Locate the cells, classifying each as a parasitized RBC, an uninfected RBC, or a WBC.
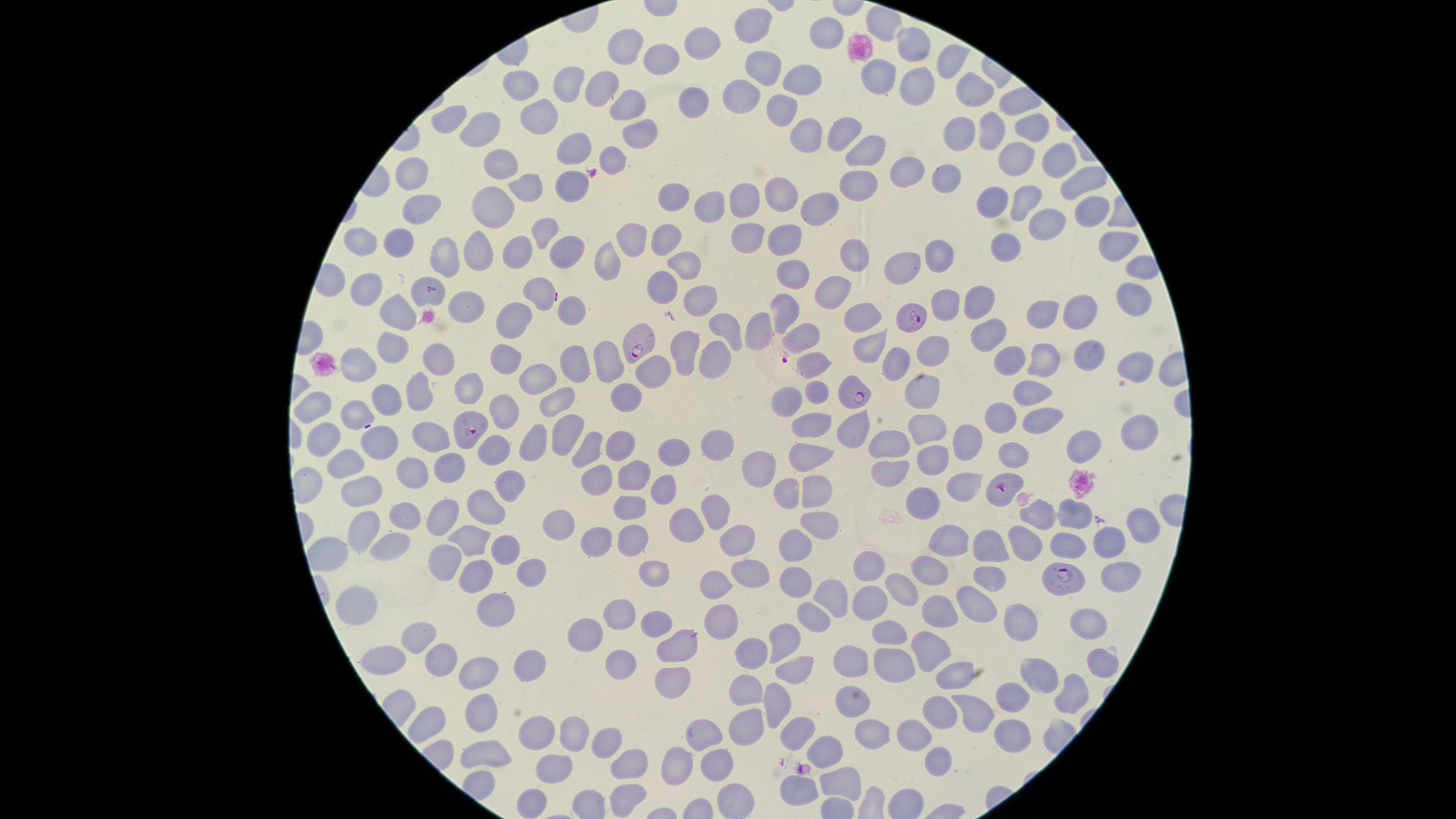

Approximate marker points, in pixels from the top-left corner.
Parasitized RBCs: (x=912, y=319), (x=646, y=343), (x=852, y=388), (x=468, y=427), (x=997, y=487), (x=1062, y=578).
Uninfected RBCs: (x=883, y=24), (x=753, y=29), (x=823, y=31), (x=696, y=45), (x=920, y=45), (x=627, y=50), (x=666, y=59), (x=948, y=60), (x=762, y=63), (x=882, y=74), (x=791, y=78), (x=916, y=81), (x=970, y=84), (x=605, y=86), (x=518, y=89), (x=562, y=91), (x=742, y=91), (x=693, y=99), (x=628, y=106), (x=781, y=111), (x=542, y=120), (x=451, y=125), (x=1030, y=125), (x=486, y=128), (x=811, y=128), (x=995, y=130), (x=841, y=131), (x=643, y=132), (x=957, y=136), (x=572, y=146), (x=869, y=150), (x=1053, y=159), (x=615, y=160), (x=1013, y=161), (x=503, y=163), (x=910, y=172), (x=412, y=175), (x=948, y=175), (x=867, y=182), (x=1074, y=182), (x=527, y=183), (x=570, y=183), (x=668, y=197), (x=781, y=197), (x=748, y=202), (x=821, y=202), (x=996, y=202), (x=1023, y=202), (x=717, y=207), (x=421, y=210), (x=496, y=211), (x=1084, y=215), (x=1042, y=223), (x=750, y=231), (x=542, y=233), (x=663, y=237), (x=403, y=238), (x=626, y=238), (x=359, y=239), (x=782, y=240), (x=1006, y=246), (x=1111, y=247), (x=475, y=250), (x=558, y=251), (x=944, y=251), (x=440, y=254), (x=513, y=255), (x=860, y=257), (x=684, y=262), (x=610, y=265), (x=908, y=266), (x=793, y=269), (x=668, y=283), (x=367, y=291), (x=837, y=291), (x=543, y=294), (x=1132, y=294), (x=431, y=298), (x=701, y=298), (x=977, y=299), (x=940, y=301), (x=461, y=304), (x=572, y=313), (x=785, y=313), (x=1049, y=314), (x=1077, y=314), (x=395, y=315), (x=861, y=315), (x=765, y=325), (x=726, y=327), (x=511, y=330), (x=991, y=331), (x=796, y=340), (x=872, y=341), (x=684, y=348), (x=387, y=349), (x=929, y=350), (x=497, y=355), (x=567, y=356), (x=1085, y=356), (x=715, y=357), (x=1042, y=358), (x=595, y=359), (x=442, y=360), (x=820, y=361), (x=1003, y=361), (x=894, y=365), (x=1134, y=366), (x=359, y=369), (x=655, y=371), (x=534, y=381), (x=915, y=386), (x=817, y=388), (x=467, y=391), (x=1031, y=392), (x=426, y=393), (x=393, y=396), (x=558, y=399), (x=626, y=401), (x=782, y=401), (x=314, y=403), (x=360, y=410), (x=506, y=411), (x=1000, y=419), (x=1038, y=419), (x=814, y=424), (x=856, y=425), (x=568, y=427), (x=934, y=428), (x=1139, y=430), (x=969, y=436), (x=326, y=441), (x=384, y=441), (x=431, y=441), (x=532, y=441), (x=891, y=441), (x=1092, y=443), (x=618, y=444), (x=494, y=446), (x=715, y=447), (x=581, y=449), (x=671, y=450), (x=813, y=454), (x=351, y=458), (x=937, y=461), (x=1014, y=461), (x=448, y=466), (x=414, y=467), (x=761, y=469), (x=889, y=470), (x=512, y=475), (x=599, y=477), (x=632, y=477), (x=664, y=484), (x=963, y=485), (x=363, y=488), (x=817, y=491), (x=924, y=494), (x=786, y=495), (x=483, y=502), (x=715, y=509), (x=1075, y=509), (x=876, y=510), (x=1045, y=510), (x=625, y=511), (x=408, y=514), (x=444, y=516), (x=565, y=520), (x=820, y=522), (x=1141, y=522), (x=362, y=524), (x=685, y=526), (x=393, y=537), (x=473, y=537), (x=593, y=537), (x=625, y=537), (x=948, y=537), (x=744, y=541), (x=1108, y=541), (x=793, y=544), (x=1029, y=544), (x=1065, y=546), (x=443, y=548), (x=505, y=549), (x=988, y=549), (x=327, y=555), (x=863, y=566), (x=528, y=567), (x=934, y=571), (x=988, y=572), (x=1115, y=574), (x=658, y=576), (x=472, y=577), (x=741, y=577), (x=793, y=581), (x=706, y=583), (x=903, y=588), (x=835, y=590), (x=865, y=600), (x=494, y=601), (x=970, y=604), (x=357, y=606), (x=616, y=612), (x=934, y=616), (x=1020, y=617), (x=716, y=618), (x=806, y=618), (x=660, y=624), (x=1089, y=624), (x=420, y=632), (x=895, y=633), (x=588, y=634), (x=676, y=640), (x=783, y=640), (x=930, y=647), (x=756, y=651), (x=847, y=652), (x=1102, y=657), (x=380, y=658), (x=449, y=658), (x=530, y=662), (x=611, y=664), (x=894, y=665), (x=484, y=669), (x=791, y=669), (x=952, y=672), (x=1041, y=673), (x=669, y=686), (x=742, y=689), (x=1069, y=693), (x=1012, y=695), (x=778, y=702), (x=848, y=704), (x=968, y=708), (x=477, y=709), (x=936, y=710), (x=430, y=717), (x=743, y=721), (x=868, y=725), (x=537, y=731), (x=572, y=731), (x=799, y=731), (x=706, y=732), (x=912, y=733), (x=1013, y=735), (x=607, y=742), (x=481, y=748), (x=825, y=755), (x=678, y=758), (x=719, y=759), (x=628, y=762), (x=933, y=762), (x=550, y=770), (x=843, y=781), (x=802, y=785), (x=618, y=791), (x=737, y=796), (x=527, y=802).
No WBCs identified.

Single field of view. Image is 1456×819 pixels. Species: Plasmodium falciparum. Giemsa stain. Thin blood smear. The visible region is circular. Photographed with a smartphone camera through the microscope eyepiece.